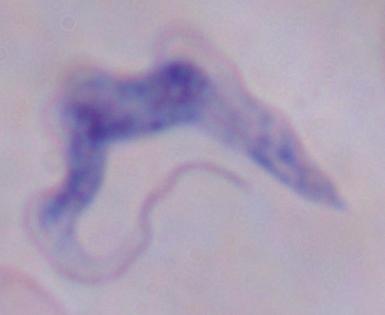

1000x magnification. Micrograph. A trypanosome is shown.